Outline each Plasmodium falciparum-infected red blood cell.
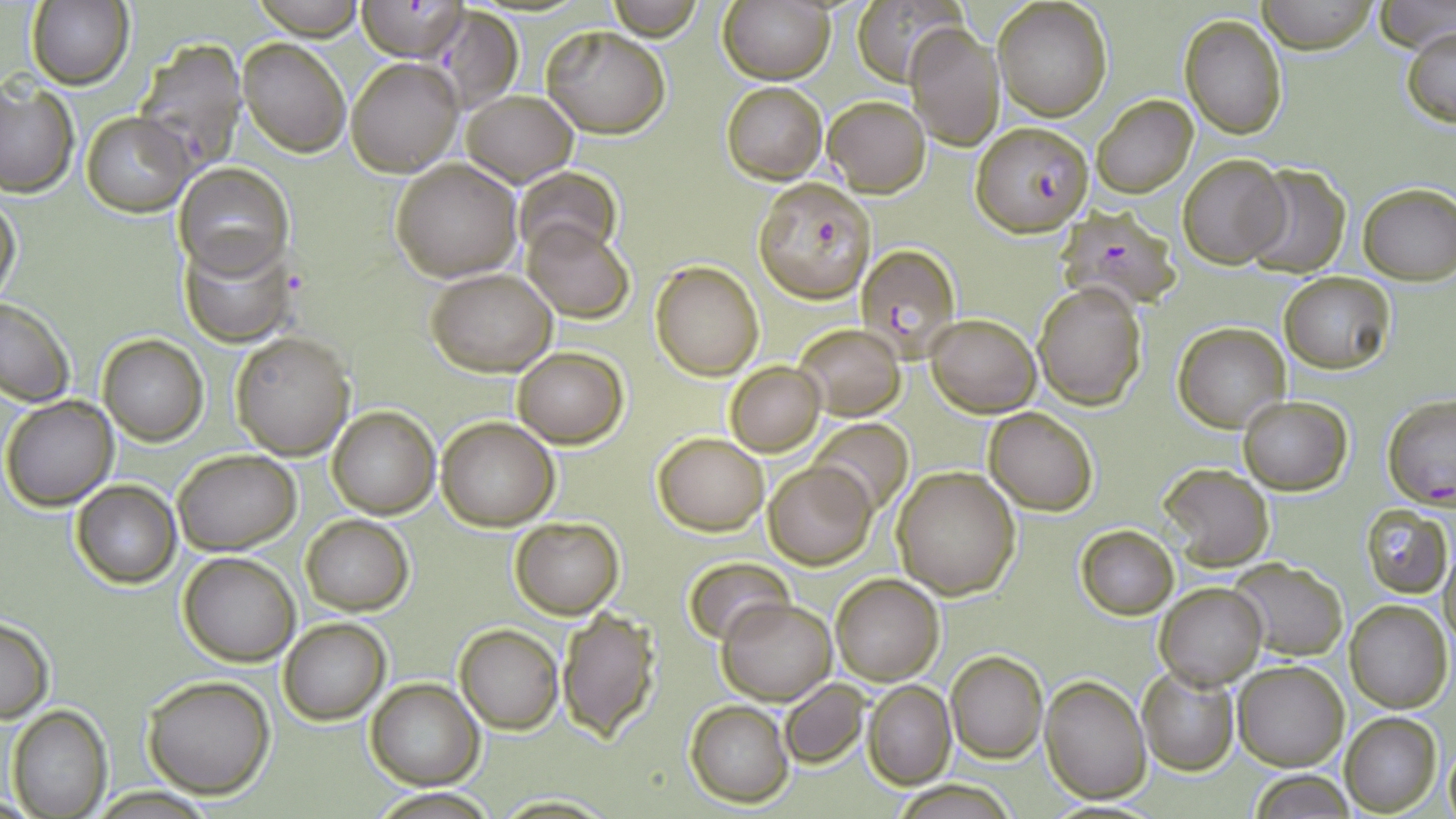
Approximate bounding boxes as [x1, y1, x2, y2] in pixels.
Plasmodium falciparum-infected red blood cells (subset): [357, 2, 468, 61], [753, 177, 876, 303], [1058, 209, 1179, 309], [856, 241, 963, 360], [1382, 396, 1456, 507].

Uninfected red blood cell locations (subset): [27, 0, 136, 91], [248, 0, 366, 41], [607, 0, 704, 40], [719, 0, 834, 84], [992, 0, 1112, 121], [1258, 0, 1377, 54], [853, 1, 964, 81], [1378, 1, 1455, 52], [429, 7, 523, 113], [1179, 14, 1287, 139], [905, 22, 1004, 150], [1403, 24, 1456, 129], [542, 25, 669, 137], [132, 35, 249, 169], [238, 37, 351, 157], [348, 58, 463, 176], [0, 80, 78, 198], [720, 81, 828, 183], [462, 90, 578, 186], [1092, 94, 1198, 200], [822, 96, 931, 197], [82, 113, 195, 216], [1177, 155, 1288, 269], [391, 157, 523, 282], [173, 162, 293, 279], [1242, 164, 1352, 277], [517, 167, 620, 258], [1359, 182, 1456, 285], [1, 192, 22, 305], [522, 220, 634, 323], [182, 232, 294, 348], [651, 261, 764, 380], [428, 268, 556, 376], [1281, 273, 1396, 374], [1032, 281, 1146, 410], [0, 297, 75, 407], [925, 314, 1040, 417], [1174, 321, 1291, 433], [795, 324, 906, 419], [231, 330, 356, 459], [97, 333, 207, 445], [513, 347, 627, 448], [725, 362, 825, 456], [1, 394, 120, 510], [1238, 396, 1352, 494], [328, 405, 440, 519], [984, 406, 1099, 515], [809, 417, 913, 517], [436, 418, 559, 530], [652, 432, 768, 535], [173, 449, 301, 556], [764, 460, 876, 569], [1158, 464, 1275, 570], [892, 466, 1020, 598], [71, 479, 181, 588], [1358, 505, 1452, 598], [301, 514, 414, 615], [510, 517, 624, 618], [1076, 525, 1179, 620], [1441, 545, 1456, 657], [178, 551, 301, 666], [683, 556, 792, 645], [1230, 559, 1349, 661], [830, 573, 944, 685], [1155, 582, 1266, 691], [717, 596, 835, 703], [1345, 601, 1452, 713], [555, 609, 662, 741], [278, 616, 391, 726], [0, 617, 54, 723], [455, 623, 563, 734], [945, 650, 1047, 763], [1233, 660, 1349, 770], [1135, 665, 1239, 774], [141, 674, 276, 799], [1041, 675, 1150, 803], [366, 679, 483, 788], [779, 679, 870, 768], [864, 681, 955, 787], [684, 699, 794, 806], [7, 705, 113, 818], [1340, 712, 1442, 816], [1443, 741, 1456, 819], [1247, 769, 1358, 818], [894, 782, 1015, 817]. Slide-level diagnosis: Plasmodium falciparum. Optical microscopy. Thin blood film. May-Grünwald-Giemsa-stained preparation. Image is 1456×819 pixels. 1000x magnification. One field of a larger specimen.